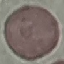

Summary:
  - Malaria status: uninfected
  - Image type: automatically extracted cell patch, resized to 64 × 64 pixels
  - Capture: smartphone through the microscope eyepiece
  - Stain: Giemsa
  - Preparation: thin blood smear